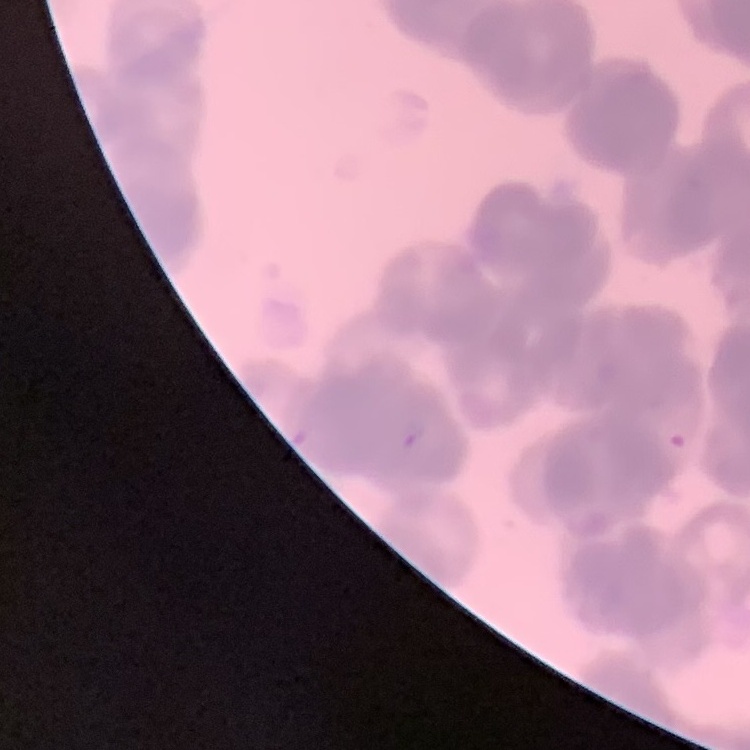
The erythrocytes exhibit rouleaux formation. Square crop of a larger photomicrograph. Thin blood smear. Field's or Giemsa stain.